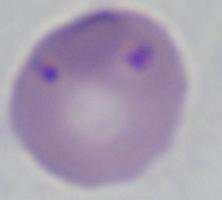

Captured at 1000x magnification. Micrograph. A Babesia parasite is seen.